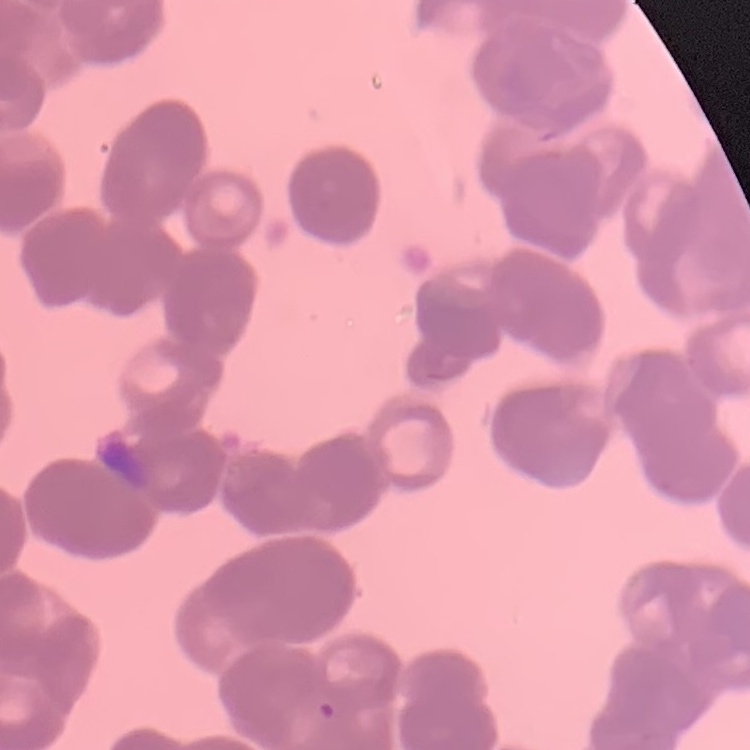

The erythrocytes exhibit rouleaux formation. One tile cut from a larger photomicrograph. Thin peripheral smear. Stained with either Field's or Giemsa.